Name the parasite shown.
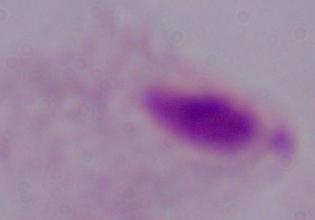

This is a trichomonad.

modality = micrograph
magnification = 1000x